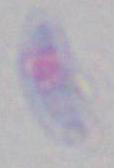
Photomicrograph. Captured at 1000x magnification. Toxoplasma gondii is seen.